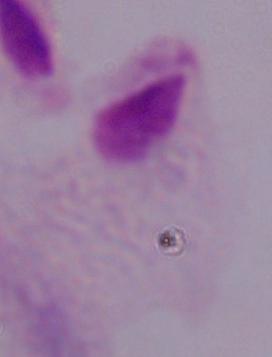

magnification = 1000x
modality = micrograph
identification = trichomonad